Mark where platelets are.
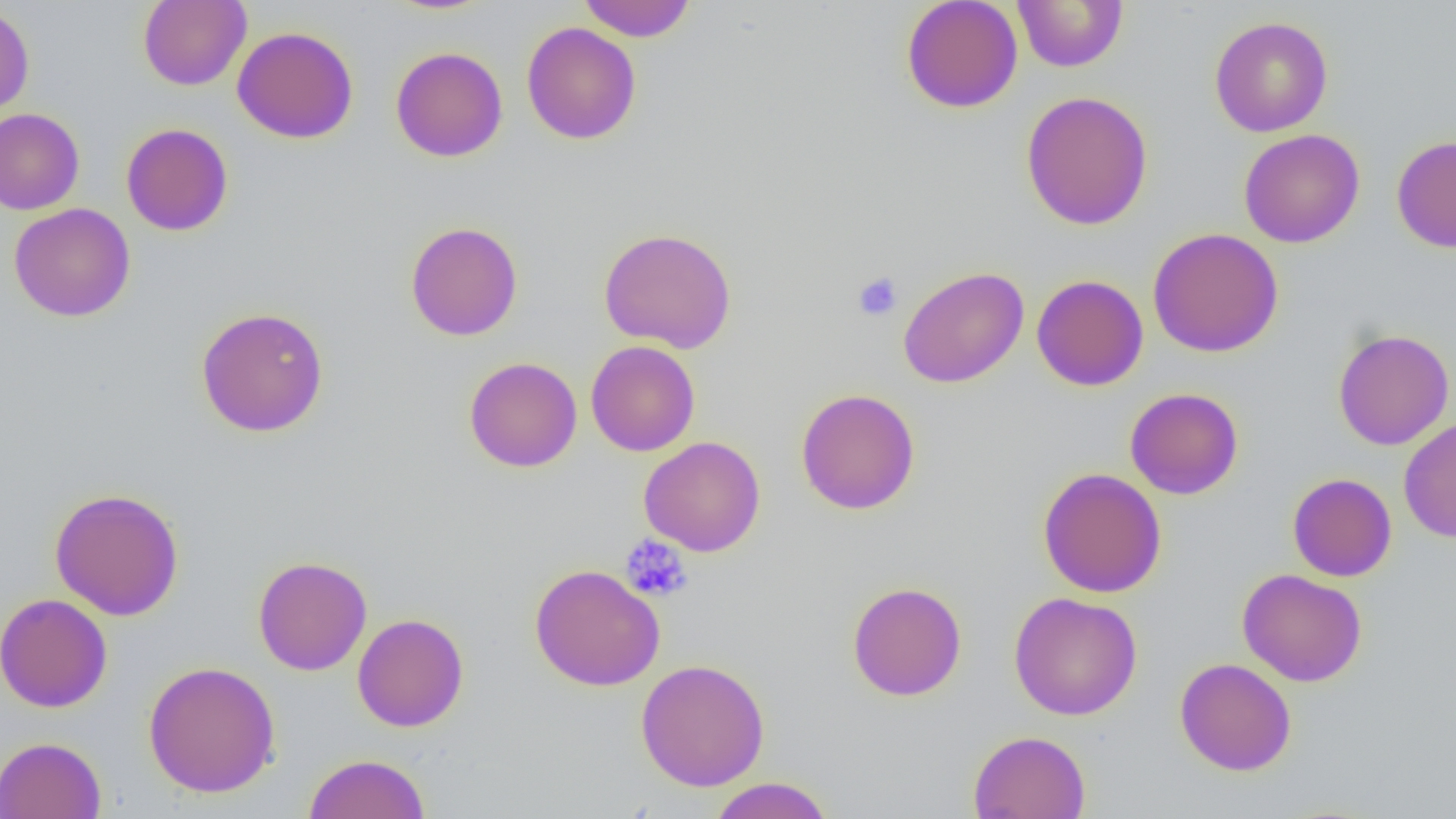

Approximate bounding boxes as (x1, y1, x2, y2) in pixels.
Platelets: (852, 272, 903, 322), (620, 535, 692, 602).

Summary:
  - Uninfected red blood cell locations: (138, 0, 252, 91), (383, 0, 497, 16), (577, 0, 696, 41), (900, 0, 1023, 113), (1012, 0, 1128, 73), (0, 3, 35, 119), (1209, 16, 1333, 137), (521, 22, 641, 144), (232, 26, 359, 143), (390, 46, 508, 162), (1021, 90, 1154, 231), (0, 108, 84, 215), (121, 123, 234, 236), (1238, 129, 1365, 248), (1391, 135, 1456, 253), (9, 203, 135, 322), (405, 221, 523, 341), (598, 227, 737, 354), (1147, 227, 1284, 358), (898, 266, 1029, 388), (1031, 275, 1148, 391), (195, 306, 330, 437), (1332, 329, 1455, 450), (585, 341, 700, 457), (464, 356, 582, 472), (795, 387, 921, 515), (1124, 387, 1243, 499), (1398, 417, 1456, 543), (638, 435, 766, 556), (1037, 467, 1167, 598), (1287, 473, 1397, 582), (49, 487, 185, 621), (253, 556, 372, 676), (529, 563, 665, 691), (1237, 568, 1368, 687), (847, 581, 967, 701), (1009, 591, 1143, 721), (0, 593, 113, 713), (352, 613, 469, 732), (634, 658, 770, 791), (1175, 658, 1297, 776), (142, 660, 281, 798), (968, 730, 1090, 819), (0, 736, 107, 819), (303, 753, 431, 819), (707, 776, 834, 819)
  - Slide-level diagnosis: negative for blood parasites
  - Preparation: thin blood smear
  - Modality: optical microscopy
  - Image size: 1456×819 pixels
  - Field of view: one of a larger specimen
  - Magnification: 1000x